Give the extent of all Plasmodium ovale-infected red blood cells.
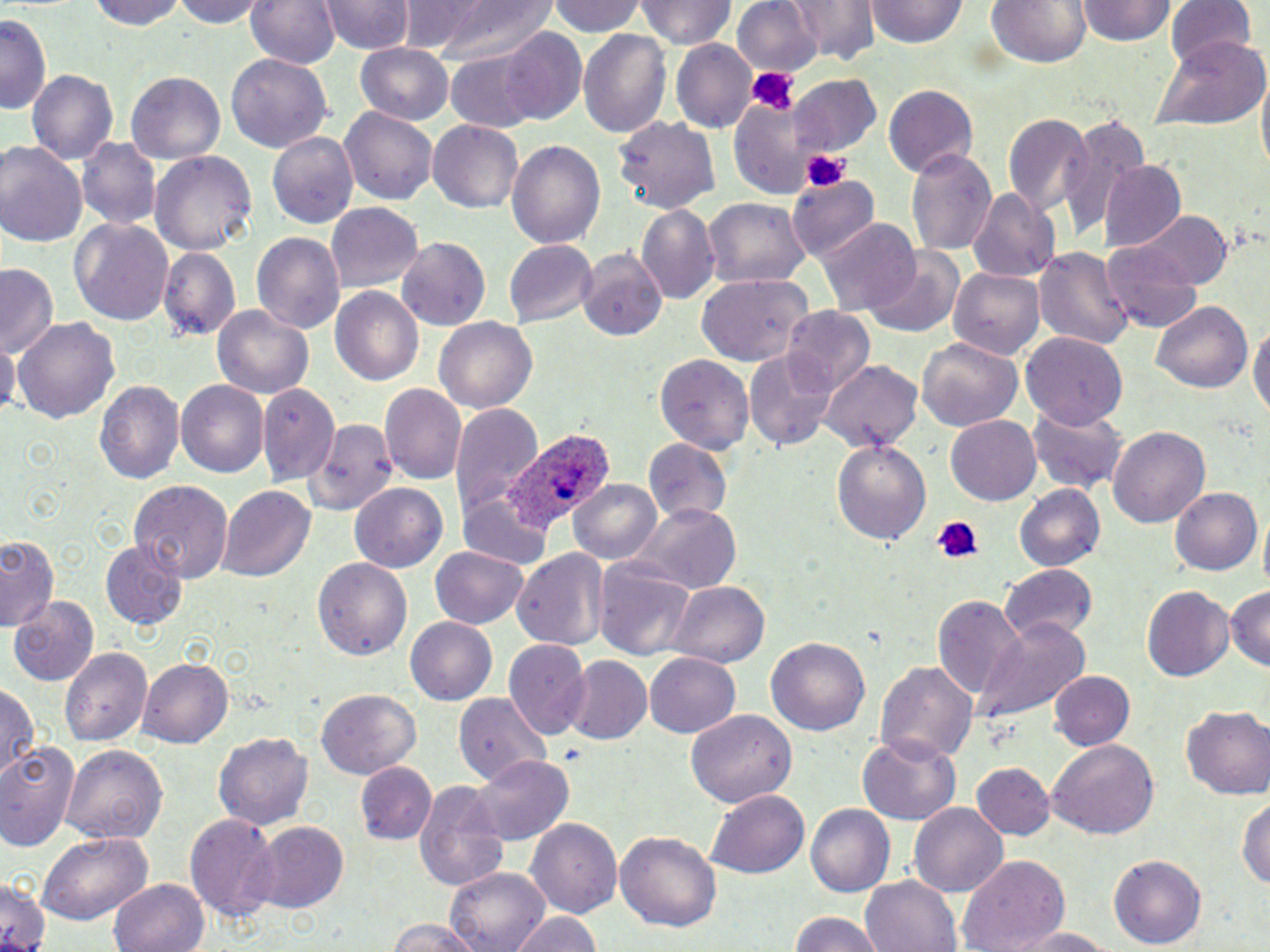

Approximate bounding boxes as named x1/y1/x2/y2 corners in pixels.
Plasmodium ovale-infected red blood cells: (x1=507, y1=429, x2=608, y2=529).

Uninfected red blood cell locations: (x1=89, y1=0, x2=188, y2=30), (x1=171, y1=0, x2=267, y2=27), (x1=243, y1=0, x2=339, y2=69), (x1=323, y1=0, x2=412, y2=55), (x1=416, y1=0, x2=558, y2=66), (x1=551, y1=0, x2=648, y2=38), (x1=639, y1=0, x2=733, y2=50), (x1=734, y1=0, x2=824, y2=79), (x1=786, y1=0, x2=879, y2=64), (x1=868, y1=0, x2=966, y2=49), (x1=1167, y1=0, x2=1257, y2=73), (x1=982, y1=1, x2=1094, y2=68), (x1=1076, y1=2, x2=1178, y2=48), (x1=0, y1=13, x2=49, y2=116), (x1=579, y1=26, x2=671, y2=138), (x1=499, y1=27, x2=587, y2=123), (x1=1155, y1=35, x2=1267, y2=133), (x1=674, y1=39, x2=756, y2=135), (x1=355, y1=41, x2=455, y2=125), (x1=447, y1=51, x2=541, y2=130), (x1=226, y1=53, x2=331, y2=153), (x1=27, y1=70, x2=117, y2=166), (x1=127, y1=70, x2=228, y2=164), (x1=790, y1=75, x2=882, y2=158), (x1=884, y1=83, x2=979, y2=178), (x1=726, y1=94, x2=818, y2=194), (x1=340, y1=107, x2=437, y2=207), (x1=1001, y1=108, x2=1092, y2=221), (x1=1059, y1=110, x2=1150, y2=237), (x1=614, y1=114, x2=721, y2=213), (x1=427, y1=119, x2=526, y2=214), (x1=265, y1=130, x2=358, y2=230), (x1=76, y1=137, x2=161, y2=232), (x1=507, y1=139, x2=606, y2=251), (x1=0, y1=141, x2=86, y2=249), (x1=906, y1=147, x2=998, y2=260), (x1=150, y1=150, x2=255, y2=258), (x1=1098, y1=160, x2=1184, y2=250), (x1=786, y1=173, x2=879, y2=261), (x1=969, y1=188, x2=1061, y2=282), (x1=702, y1=197, x2=812, y2=290), (x1=326, y1=202, x2=424, y2=292), (x1=636, y1=204, x2=719, y2=303), (x1=1135, y1=211, x2=1231, y2=292), (x1=69, y1=218, x2=175, y2=328), (x1=815, y1=220, x2=921, y2=317), (x1=251, y1=231, x2=344, y2=337), (x1=394, y1=236, x2=491, y2=332), (x1=503, y1=239, x2=596, y2=327), (x1=1099, y1=241, x2=1203, y2=334), (x1=1036, y1=243, x2=1134, y2=354), (x1=160, y1=248, x2=239, y2=343), (x1=579, y1=248, x2=667, y2=342), (x1=864, y1=250, x2=964, y2=337), (x1=0, y1=263, x2=60, y2=360), (x1=949, y1=267, x2=1044, y2=361), (x1=695, y1=270, x2=814, y2=366), (x1=329, y1=286, x2=425, y2=386), (x1=1150, y1=300, x2=1252, y2=395), (x1=211, y1=305, x2=314, y2=399), (x1=783, y1=307, x2=875, y2=392), (x1=433, y1=314, x2=537, y2=411), (x1=13, y1=317, x2=121, y2=424), (x1=1249, y1=318, x2=1269, y2=428), (x1=1022, y1=330, x2=1126, y2=427), (x1=1, y1=337, x2=19, y2=421), (x1=917, y1=338, x2=1023, y2=431), (x1=743, y1=347, x2=840, y2=450), (x1=653, y1=352, x2=753, y2=455), (x1=820, y1=360, x2=924, y2=455), (x1=93, y1=380, x2=183, y2=487), (x1=176, y1=381, x2=268, y2=477), (x1=256, y1=385, x2=336, y2=482), (x1=379, y1=386, x2=464, y2=486), (x1=450, y1=403, x2=543, y2=527), (x1=1026, y1=404, x2=1129, y2=497), (x1=946, y1=415, x2=1041, y2=502), (x1=308, y1=416, x2=397, y2=519), (x1=1109, y1=426, x2=1212, y2=528), (x1=831, y1=434, x2=932, y2=545), (x1=643, y1=437, x2=734, y2=526), (x1=568, y1=478, x2=664, y2=565), (x1=129, y1=481, x2=232, y2=579), (x1=351, y1=481, x2=448, y2=574), (x1=1014, y1=484, x2=1106, y2=573), (x1=219, y1=485, x2=313, y2=582), (x1=1169, y1=487, x2=1260, y2=577), (x1=459, y1=497, x2=544, y2=565), (x1=628, y1=504, x2=743, y2=593), (x1=0, y1=533, x2=59, y2=630), (x1=100, y1=540, x2=187, y2=628), (x1=430, y1=547, x2=529, y2=629), (x1=512, y1=547, x2=610, y2=654), (x1=314, y1=556, x2=413, y2=662), (x1=595, y1=558, x2=699, y2=665), (x1=995, y1=564, x2=1097, y2=642), (x1=668, y1=580, x2=771, y2=668), (x1=1142, y1=584, x2=1234, y2=682), (x1=1225, y1=585, x2=1269, y2=673), (x1=931, y1=593, x2=1026, y2=708), (x1=10, y1=597, x2=100, y2=686), (x1=973, y1=616, x2=1089, y2=726), (x1=405, y1=617, x2=497, y2=705), (x1=766, y1=638, x2=870, y2=737), (x1=504, y1=639, x2=590, y2=738), (x1=58, y1=645, x2=150, y2=748), (x1=644, y1=651, x2=742, y2=737), (x1=566, y1=656, x2=652, y2=744), (x1=139, y1=657, x2=234, y2=747), (x1=878, y1=659, x2=976, y2=768), (x1=1048, y1=671, x2=1134, y2=752), (x1=2, y1=680, x2=38, y2=783), (x1=316, y1=690, x2=421, y2=777), (x1=454, y1=692, x2=550, y2=782), (x1=1181, y1=706, x2=1269, y2=799), (x1=686, y1=709, x2=794, y2=810), (x1=214, y1=731, x2=313, y2=831), (x1=858, y1=736, x2=960, y2=825), (x1=0, y1=738, x2=81, y2=851), (x1=1047, y1=739, x2=1159, y2=841), (x1=64, y1=745, x2=169, y2=844), (x1=473, y1=753, x2=572, y2=845), (x1=972, y1=762, x2=1054, y2=839), (x1=356, y1=763, x2=435, y2=845), (x1=413, y1=779, x2=507, y2=891), (x1=706, y1=789, x2=809, y2=881), (x1=1237, y1=792, x2=1270, y2=892), (x1=911, y1=802, x2=1006, y2=897), (x1=805, y1=804, x2=894, y2=898), (x1=187, y1=811, x2=281, y2=927), (x1=526, y1=818, x2=622, y2=917), (x1=252, y1=822, x2=350, y2=914), (x1=616, y1=830, x2=720, y2=933), (x1=35, y1=832, x2=154, y2=924), (x1=957, y1=854, x2=1072, y2=952), (x1=1108, y1=854, x2=1205, y2=950), (x1=446, y1=865, x2=550, y2=952), (x1=0, y1=873, x2=53, y2=952), (x1=861, y1=875, x2=962, y2=952), (x1=109, y1=876, x2=209, y2=952), (x1=510, y1=910, x2=604, y2=952), (x1=786, y1=911, x2=887, y2=952), (x1=384, y1=919, x2=481, y2=952), (x1=1003, y1=925, x2=1120, y2=950). Platelet locations: (x1=743, y1=64, x2=798, y2=116), (x1=801, y1=148, x2=851, y2=194), (x1=929, y1=515, x2=986, y2=566). Slide-level diagnosis: Plasmodium ovale. May-Grünwald-Giemsa-stained preparation. Thin blood smear. Optical microscopy. One field of a larger specimen. Captured at 1000x magnification. Image is 1270×952 pixels.